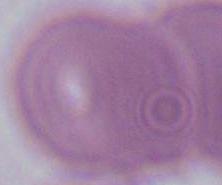
magnification = 1000x
modality = micrograph
identification = red blood cell